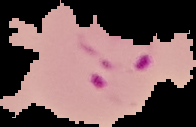
image_size: 196×127 pixels
preparation: thin blood film
image_type: segmented cell region on a black background
result: Plasmodium parasites identified